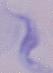

modality: photomicrograph
identification: trypanosome
magnification: 1000x